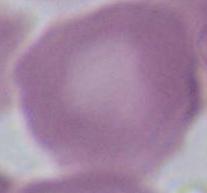
Captured at 1000x magnification. Photomicrograph. A red blood cell is shown.